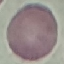

Summary:
  - Malaria status: uninfected
  - Stain: Giemsa
  - Capture: smartphone through the microscope eyepiece
  - Preparation: thin blood smear
  - Image type: cell patch, automatically extracted from a larger field of view and resized to 64 × 64 pixels